Identify the blood parasite species.
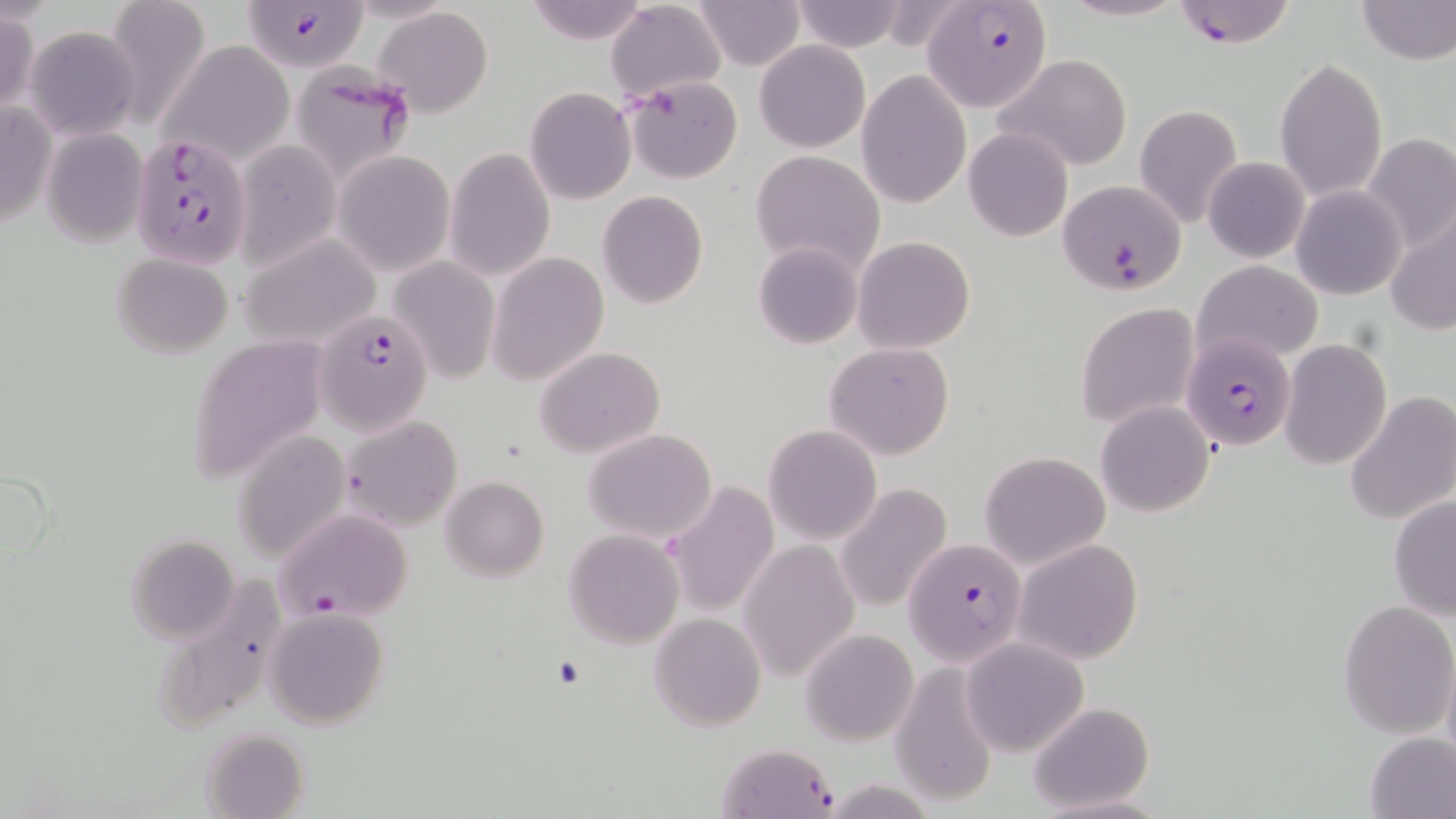
Plasmodium falciparum.

{
  "image_size": "1456×819 pixels",
  "stain": "May-Grünwald-Giemsa",
  "field_of_view": "single",
  "magnification": "1000x",
  "uninfected_red_blood_cell_locations": "approximate bounding boxes as (x1,y1)-(x2,y2) corner pairs in pixels: (101,0)-(212,127), (521,0)-(654,46), (691,0)-(807,70), (790,0)-(910,53), (1057,0)-(1189,23), (1354,0)-(1455,65), (606,2)-(725,103), (373,7)-(495,116), (0,8)-(38,117), (25,26)-(141,138), (159,40)-(295,164), (754,40)-(870,152), (993,54)-(1134,172), (1275,57)-(1388,202), (291,65)-(418,187), (856,69)-(971,210), (624,75)-(743,182), (523,86)-(636,205), (1,93)-(53,238), (1133,105)-(1243,228), (43,128)-(147,246), (962,128)-(1073,242), (1364,132)-(1456,257), (234,139)-(339,267), (444,147)-(556,281), (751,149)-(885,277), (332,150)-(455,276), (1203,156)-(1309,264), (1291,185)-(1407,299), (596,190)-(708,309), (1385,207)-(1456,339), (241,234)-(380,348), (852,236)-(976,354), (754,242)-(862,349), (112,252)-(233,359), (488,252)-(610,385), (389,255)-(500,385), (1194,260)-(1323,364), (1076,301)-(1199,427), (190,336)-(329,478), (1280,339)-(1392,469), (824,342)-(956,461), (535,347)-(665,459), (1344,389)-(1455,526), (1095,401)-(1214,515), (340,415)-(462,533), (763,424)-(882,544), (583,428)-(719,542), (233,431)-(350,563), (978,451)-(1110,569), (442,475)-(549,582), (660,480)-(778,617), (836,483)-(952,614), (1388,493)-(1456,622), (564,529)-(685,649), (128,535)-(240,643), (736,535)-(862,684), (1013,540)-(1144,664), (1338,599)-(1456,738), (265,608)-(388,729), (650,611)-(765,732), (801,627)-(918,746), (961,636)-(1089,757), (887,666)-(997,807), (1026,702)-(1156,813), (199,728)-(308,816), (1362,732)-(1456,819), (716,742)-(840,818)",
  "modality": "optical microscopy",
  "plasmodium_falciparum_infected_red_blood_cell_locations": "approximate bounding boxes as (x1,y1)-(x2,y2) corner pairs in pixels: (1169,0)-(1299,48), (241,1)-(367,72), (922,1)-(1050,110), (131,133)-(253,268), (1055,179)-(1186,294), (316,309)-(433,433), (1188,327)-(1294,456), (276,508)-(413,626), (903,538)-(1026,665)",
  "preparation": "thin blood smear"
}